Describe the morphology of the erythrocytes.
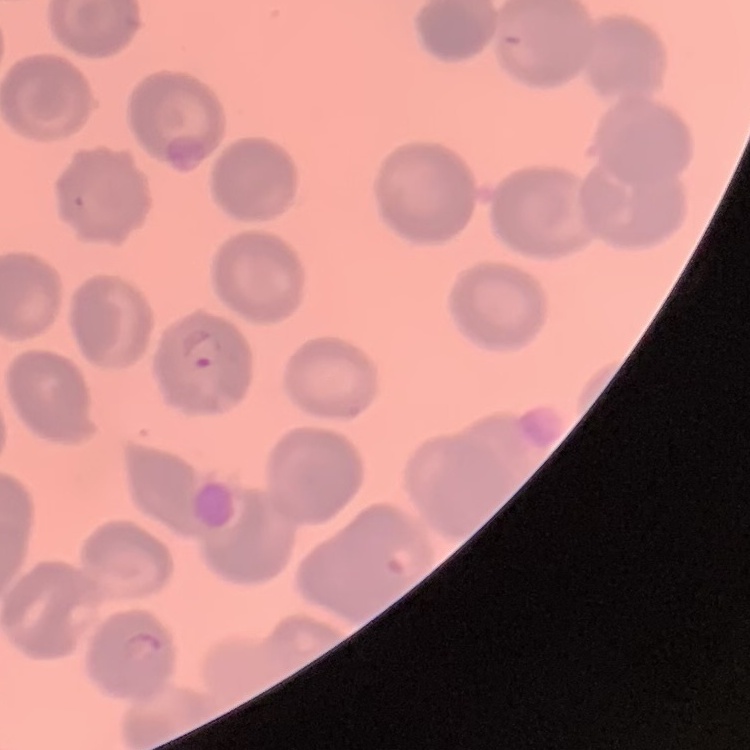

They show no rouleaux formation.

One tile cut from a larger photomicrograph. Stained with either Field's or Giemsa. Thin blood film.